Report the malaria status of this cell.
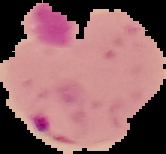

Parasitized.

The area outside the segmented cell region is set to black. Image is 166×154 pixels. From a thin blood film.